Classify this cell by malaria status.
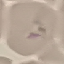
Uninfected.

{
  "preparation": "thin smear",
  "stain": "Giemsa",
  "image_type": "automatically extracted cell patch, resized to 64 × 64 pixels",
  "capture": "smartphone through the microscope eyepiece"
}